Assess this cell for malaria.
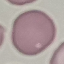
It is uninfected.

stain: Giemsa
preparation: thin smear
image_type: automatically extracted cell patch, resized to 64 × 64 pixels
capture: smartphone camera at the microscope eyepiece